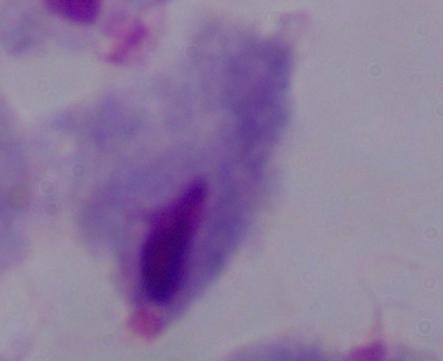
1000x magnification. A trichomonad is seen. Micrograph.